Describe the morphology of the red blood cells.
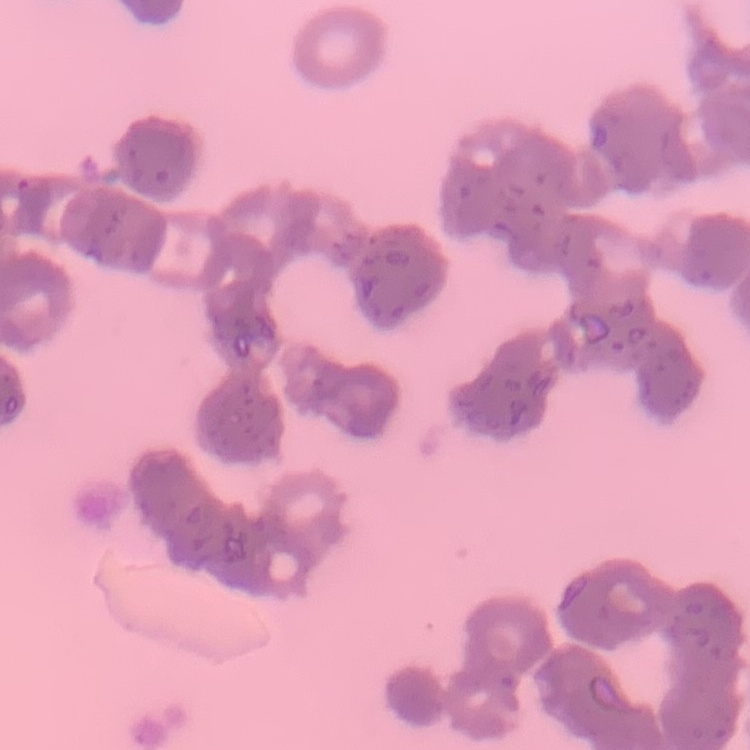
Rouleaux formation.

Field's or Giemsa stain. Thin peripheral smear. One tile cut from a larger photomicrograph.